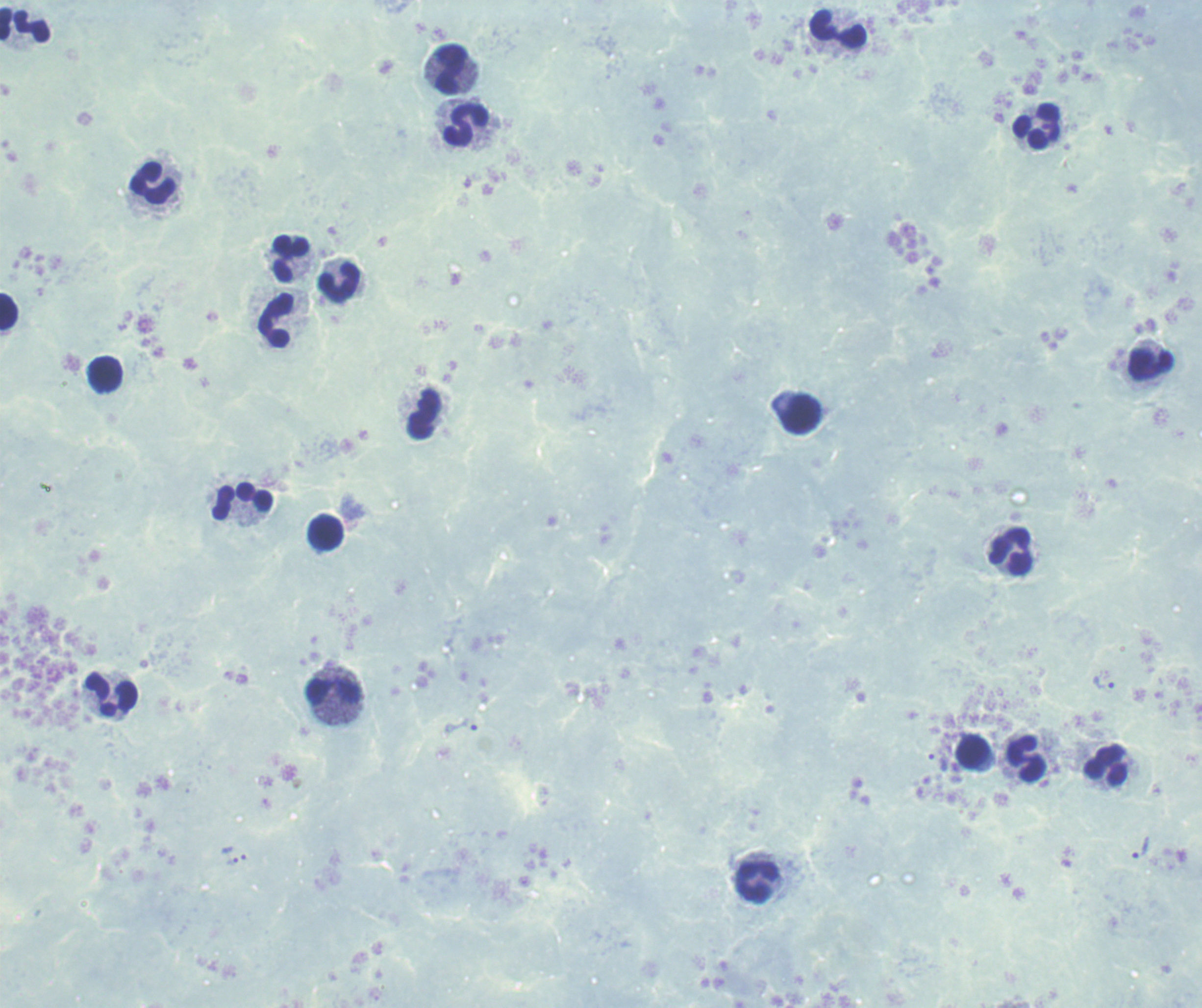 Approximate centers as [x, y] in pixels. Leukocyte locations: [25, 25], [838, 30], [450, 70], [466, 125], [1038, 127], [153, 185], [291, 259], [339, 282], [9, 313], [277, 320], [1151, 365], [105, 374], [425, 414], [801, 414], [243, 502], [327, 532], [1011, 553], [335, 691], [111, 694], [973, 753], [1027, 759], [1106, 764], [757, 883]. Trophozoite locations: [1104, 684], [465, 726], [1140, 848], [231, 855]. One field from this slide. Thick smear of blood. Previously used in an actual diagnosis. Background quality: unsatisfactory. Captured at 100x magnification. Romanowsky stain. Result: positive for Plasmodium parasites. Image is 1202×1008 pixels.